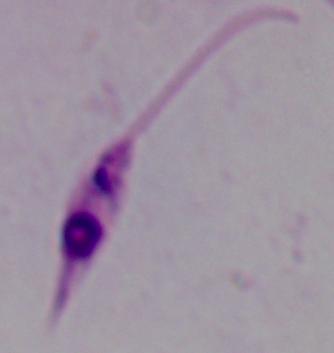

magnification = 1000x
modality = photomicrograph
identification = Leishmania